Locate and identify every blood parasite.
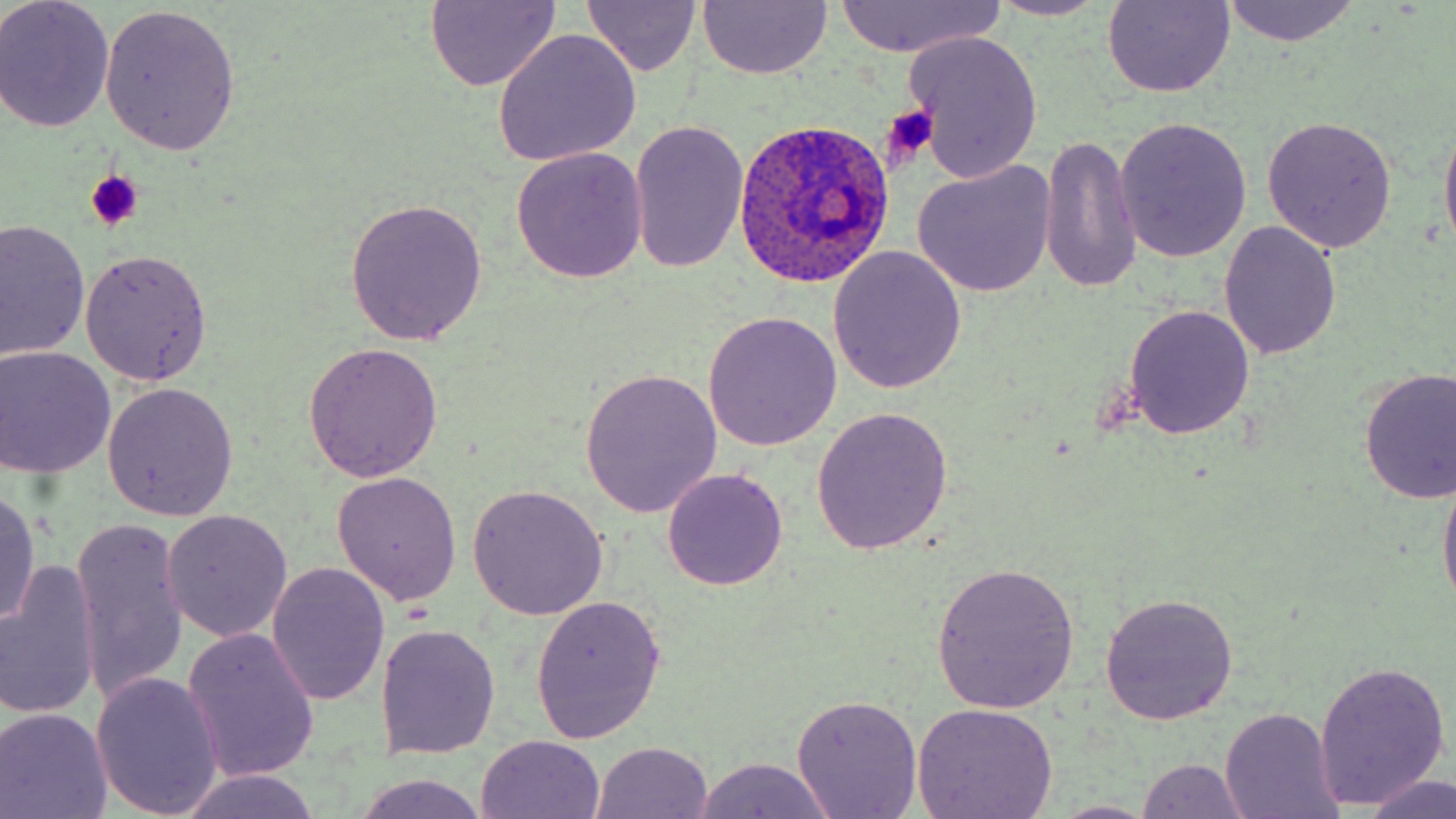

Approximate bounding boxes as (x1, y1, x2, y2) in pixels.
Plasmodium ovale-infected red blood cells: (733, 119, 895, 289).
No Plasmodium falciparum, Plasmodium malariae, Plasmodium vivax, Babesia divergens, or Trypanosoma brucei observed.

Summary:
  - Platelet locations: (880, 107, 938, 165), (85, 170, 144, 231)
  - Uninfected red blood cell locations: (0, 0, 116, 132), (983, 0, 1114, 22), (424, 1, 562, 90), (1100, 1, 1237, 98), (1219, 1, 1361, 46), (697, 2, 832, 80), (829, 2, 1006, 57), (582, 3, 704, 77), (99, 4, 241, 153), (492, 29, 642, 166), (903, 31, 1046, 184), (1438, 109, 1456, 265), (1262, 116, 1397, 254), (1115, 117, 1252, 263), (627, 122, 748, 274), (1038, 136, 1144, 294), (511, 147, 648, 284), (912, 161, 1057, 298), (347, 198, 489, 345), (1, 218, 90, 366), (1219, 221, 1342, 360), (828, 246, 967, 395), (80, 249, 213, 386), (1123, 304, 1256, 440), (703, 310, 843, 452), (301, 343, 442, 483), (0, 346, 116, 478), (1356, 367, 1456, 505), (580, 368, 722, 517), (102, 382, 239, 521), (810, 405, 954, 553), (1438, 463, 1456, 616), (663, 469, 786, 589), (330, 470, 463, 605), (467, 485, 609, 619), (0, 488, 42, 630), (160, 512, 293, 644), (71, 520, 191, 705), (929, 560, 1081, 712), (1, 561, 101, 723), (267, 564, 390, 705), (1098, 592, 1238, 723), (530, 596, 667, 745), (376, 624, 501, 758), (182, 627, 321, 784), (1315, 660, 1451, 810), (91, 672, 224, 817), (791, 694, 924, 819), (910, 703, 1061, 819), (0, 706, 113, 819), (1217, 707, 1343, 819), (476, 734, 605, 818), (591, 742, 714, 819), (689, 756, 840, 818), (1135, 758, 1254, 818), (176, 769, 323, 818), (350, 772, 493, 819), (1362, 774, 1456, 819), (1047, 800, 1160, 818)
  - Slide-level diagnosis: Plasmodium ovale
  - Preparation: thin blood smear
  - Image size: 1456×819 pixels
  - Modality: light microscopy
  - Field of view: one of a larger specimen
  - Magnification: 1000x
  - Stain: May-Grünwald-Giemsa